Assess this cell for malaria.
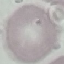
It is uninfected.

Summary:
  - Preparation: thin blood film
  - Stain: Giemsa
  - Image type: automatically extracted cell patch, resized to 64 × 64 pixels
  - Capture: smartphone camera at the microscope eyepiece